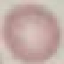

Result: no malaria parasites detected. Acquired by smartphone through the microscope eyepiece. Thin blood smear. Giemsa stain. Automatically extracted cell patch, resized to 64 × 64 pixels.